Assess the morphology of the erythrocytes.
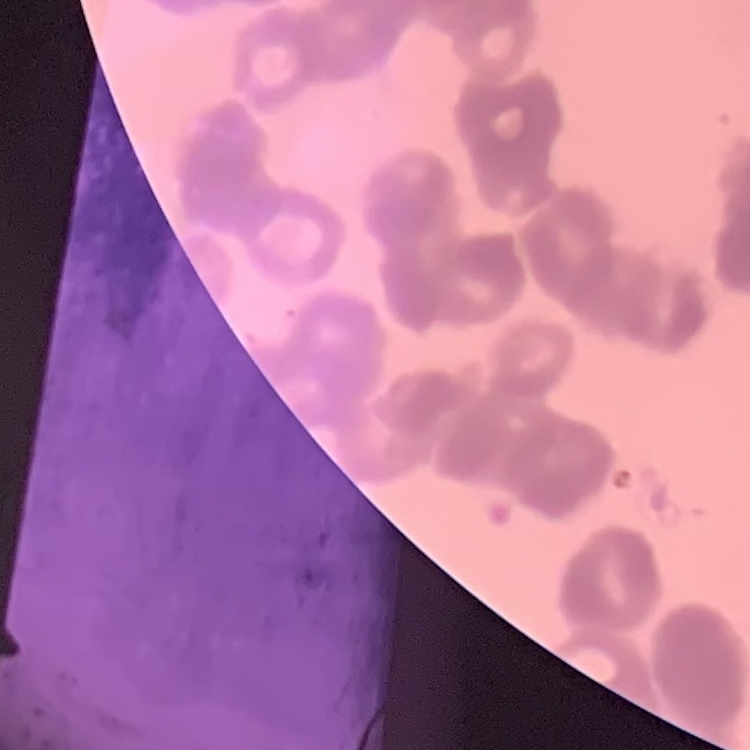

Rouleaux formation.

{
  "preparation": "thin blood smear",
  "image_type": "square crop of a larger photomicrograph",
  "stain": "Field's or Giemsa"
}